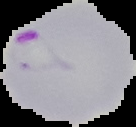
image_type: segmented cell region with the area outside set to black
image_size: 136×127 pixels
result: malaria parasites identified
preparation: thin blood smear